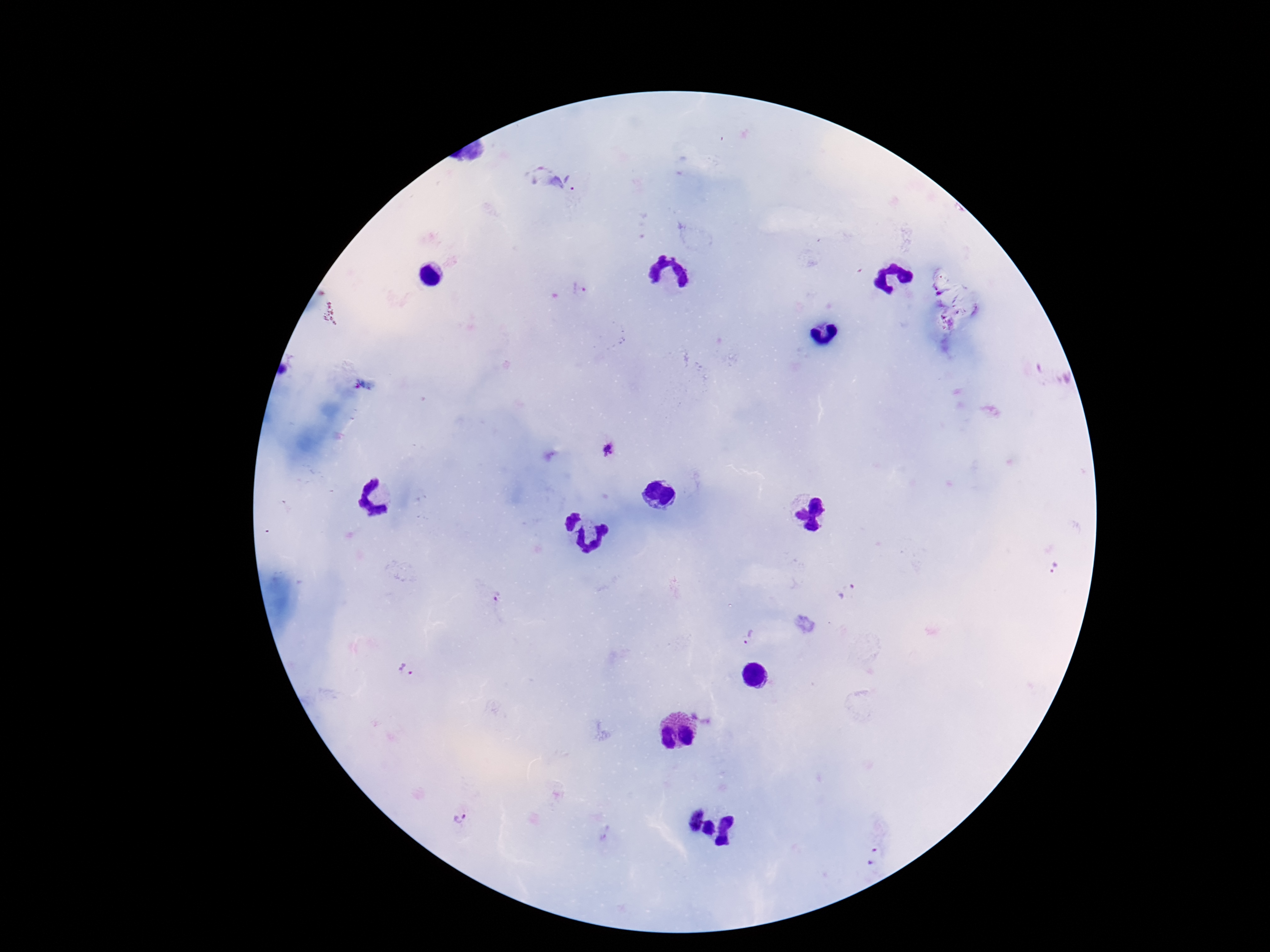
Approximate centers as [x, y] in pixels.
Summary:
  - Plasmodium parasite locations: [550, 178], [581, 292], [606, 449], [1052, 566], [849, 590], [498, 597], [750, 636], [407, 669], [461, 818], [875, 856]
  - Image size: 1270×952 pixels
  - Capture: smartphone camera through the microscope eyepiece
  - Preparation: thick peripheral-blood smear
  - Field of view: single
  - Magnification: 100x
  - Stain: Giemsa
  - Patient malaria status: infected